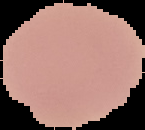 Cell region segmented out of the field of view; the surrounding area is masked to black. From a thin blood film. Image is 145×130 pixels. Malaria status: uninfected.